Locate every blood parasite and identify its species.
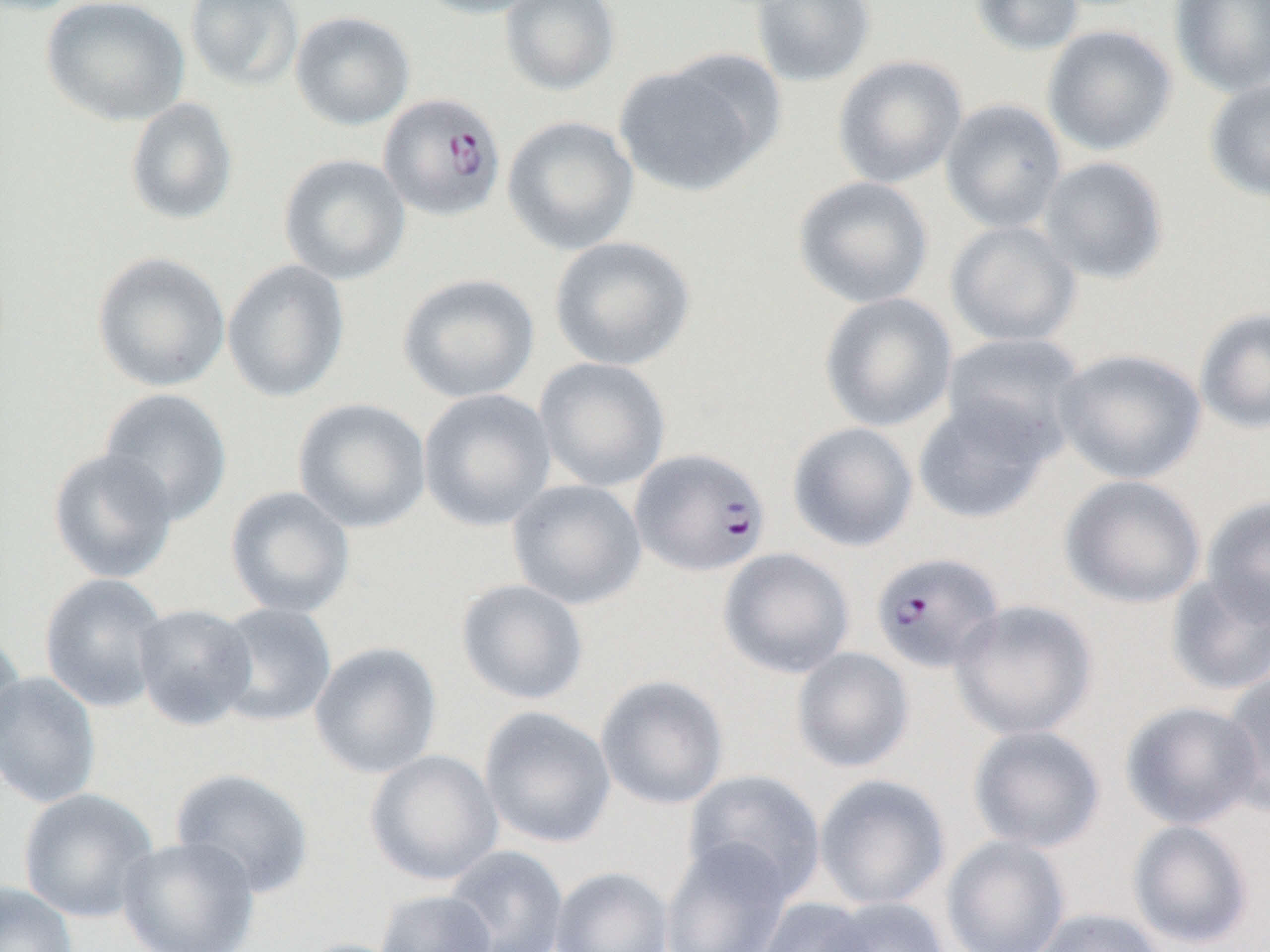

Approximate bounding boxes as (x1, y1, x2, y2) in pixels.
Plasmodium falciparum-infected red blood cells: (378, 92, 506, 222), (630, 447, 771, 578), (870, 552, 1005, 673).
No Plasmodium ovale, Plasmodium malariae, Plasmodium vivax, Babesia divergens, or Trypanosoma brucei observed.

slide_level_diagnosis: Plasmodium falciparum
modality: light microscopy
magnification: 1000x
image_size: 1270×952 pixels
preparation: thin blood film
uninfected_red_blood_cell_locations: 'approximate bounding boxes as (x1, y1, x2, y2) in pixels: (40, 0, 190, 127), (184, 0, 303, 91), (410, 0, 550, 19), (499, 0, 621, 96), (749, 0, 876, 88), (969, 0, 1085, 57), (1169, 1, 1270, 99), (290, 10, 416, 130), (1042, 24, 1178, 157), (832, 55, 968, 189), (613, 59, 772, 197), (1203, 78, 1270, 204), (125, 97, 239, 226), (940, 98, 1067, 233), (502, 115, 639, 256), (278, 153, 411, 285), (1038, 156, 1170, 285), (792, 176, 934, 309), (945, 220, 1082, 348), (548, 235, 696, 372), (92, 251, 231, 393), (222, 258, 351, 403), (397, 272, 540, 404), (818, 292, 958, 432), (1194, 306, 1270, 435), (939, 332, 1087, 459), (1054, 348, 1207, 485), (534, 357, 672, 492), (98, 388, 233, 526), (418, 388, 557, 532), (912, 396, 1056, 524), (292, 398, 432, 534), (787, 422, 919, 552), (46, 448, 179, 584), (1059, 474, 1206, 609), (507, 478, 647, 610), (224, 485, 356, 619), (1201, 496, 1270, 627), (718, 547, 855, 679), (1164, 572, 1270, 697), (39, 573, 170, 713), (455, 578, 590, 705), (949, 599, 1099, 741), (211, 602, 337, 727), (133, 603, 258, 729), (0, 627, 25, 757), (309, 642, 444, 779), (791, 647, 915, 773), (1219, 670, 1270, 817), (0, 671, 102, 810), (595, 674, 730, 810), (1121, 700, 1264, 829), (479, 706, 617, 849), (967, 724, 1106, 853), (364, 749, 504, 886), (170, 767, 315, 899), (683, 769, 827, 902), (814, 773, 951, 910), (18, 788, 160, 923), (1127, 819, 1255, 950), (116, 835, 260, 952), (940, 835, 1071, 952), (660, 838, 794, 952), (443, 845, 569, 952), (550, 866, 675, 952), (0, 880, 79, 952), (374, 889, 498, 952), (814, 896, 953, 952), (753, 898, 879, 952), (1029, 907, 1169, 952), (293, 938, 417, 952)'
field_of_view: single